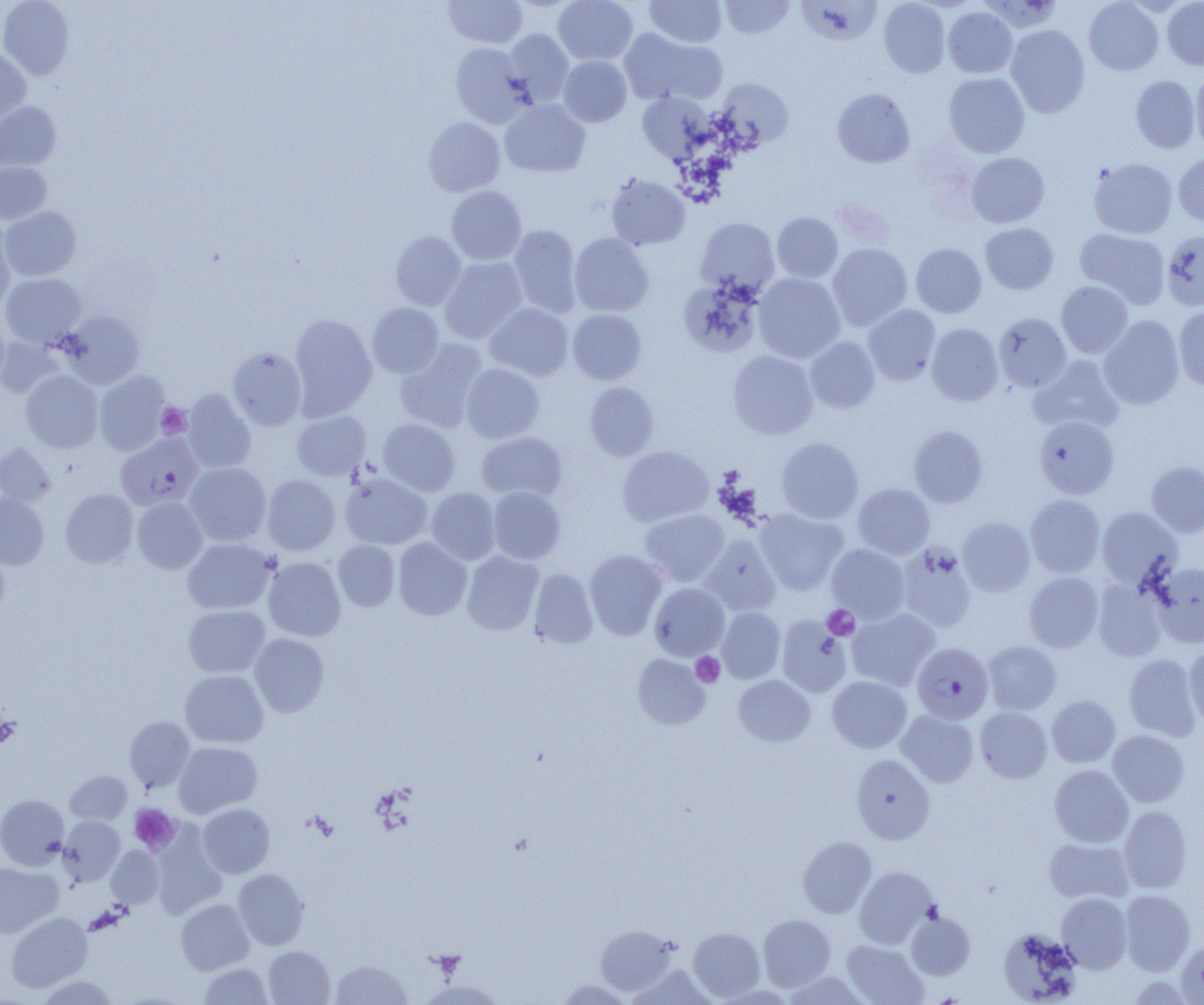 Approximate bounding boxes as named x1/y1/x2/y2 corners in pixels. Platelet locations: (x1=156, y1=403, x2=191, y2=439), (x1=822, y1=605, x2=859, y2=640), (x1=691, y1=652, x2=725, y2=687), (x1=0, y1=715, x2=20, y2=748), (x1=129, y1=804, x2=180, y2=854). Uninfected red blood cell locations: (x1=0, y1=0, x2=74, y2=80), (x1=444, y1=0, x2=527, y2=48), (x1=553, y1=0, x2=637, y2=65), (x1=645, y1=0, x2=726, y2=48), (x1=720, y1=0, x2=794, y2=38), (x1=879, y1=0, x2=950, y2=77), (x1=1084, y1=0, x2=1164, y2=76), (x1=797, y1=1, x2=881, y2=45), (x1=1162, y1=1, x2=1204, y2=70), (x1=943, y1=7, x2=1017, y2=78), (x1=1006, y1=25, x2=1090, y2=117), (x1=618, y1=28, x2=726, y2=107), (x1=504, y1=29, x2=574, y2=105), (x1=449, y1=43, x2=533, y2=127), (x1=0, y1=48, x2=31, y2=126), (x1=558, y1=55, x2=632, y2=127), (x1=1191, y1=69, x2=1204, y2=152), (x1=943, y1=72, x2=1030, y2=158), (x1=1131, y1=76, x2=1201, y2=154), (x1=716, y1=78, x2=794, y2=148), (x1=832, y1=88, x2=915, y2=168), (x1=637, y1=92, x2=712, y2=162), (x1=499, y1=99, x2=590, y2=177), (x1=0, y1=101, x2=61, y2=171), (x1=423, y1=117, x2=505, y2=196), (x1=966, y1=153, x2=1049, y2=228), (x1=1173, y1=153, x2=1204, y2=227), (x1=1089, y1=158, x2=1177, y2=239), (x1=0, y1=162, x2=52, y2=224), (x1=606, y1=173, x2=690, y2=251), (x1=446, y1=186, x2=527, y2=265), (x1=1, y1=206, x2=81, y2=281), (x1=772, y1=212, x2=843, y2=282), (x1=695, y1=217, x2=780, y2=297), (x1=0, y1=220, x2=15, y2=311), (x1=980, y1=223, x2=1058, y2=294), (x1=508, y1=225, x2=582, y2=318), (x1=1075, y1=228, x2=1170, y2=308), (x1=1161, y1=230, x2=1204, y2=311), (x1=390, y1=231, x2=466, y2=310), (x1=569, y1=233, x2=654, y2=317), (x1=827, y1=243, x2=913, y2=330), (x1=911, y1=243, x2=986, y2=318), (x1=439, y1=256, x2=528, y2=343), (x1=1, y1=273, x2=86, y2=347), (x1=753, y1=273, x2=845, y2=363), (x1=679, y1=277, x2=764, y2=358), (x1=1056, y1=281, x2=1133, y2=358), (x1=367, y1=303, x2=443, y2=378), (x1=485, y1=303, x2=574, y2=381), (x1=863, y1=305, x2=941, y2=385), (x1=1174, y1=306, x2=1204, y2=392), (x1=567, y1=309, x2=647, y2=385), (x1=578, y1=309, x2=652, y2=459), (x1=61, y1=310, x2=145, y2=388), (x1=289, y1=313, x2=377, y2=420), (x1=993, y1=313, x2=1071, y2=392), (x1=1098, y1=315, x2=1184, y2=409), (x1=0, y1=316, x2=9, y2=390), (x1=926, y1=323, x2=1003, y2=406), (x1=0, y1=335, x2=63, y2=398), (x1=805, y1=336, x2=880, y2=413), (x1=395, y1=340, x2=488, y2=432), (x1=228, y1=347, x2=307, y2=430), (x1=727, y1=350, x2=818, y2=439), (x1=1029, y1=355, x2=1124, y2=434), (x1=461, y1=363, x2=545, y2=443), (x1=21, y1=370, x2=103, y2=453), (x1=94, y1=371, x2=171, y2=455), (x1=585, y1=381, x2=659, y2=460), (x1=181, y1=389, x2=256, y2=473), (x1=292, y1=411, x2=370, y2=480), (x1=1034, y1=416, x2=1119, y2=499), (x1=378, y1=419, x2=460, y2=496), (x1=909, y1=425, x2=988, y2=507), (x1=476, y1=431, x2=567, y2=502), (x1=777, y1=437, x2=864, y2=523), (x1=0, y1=443, x2=55, y2=506), (x1=617, y1=446, x2=714, y2=526), (x1=1146, y1=460, x2=1204, y2=537), (x1=184, y1=462, x2=271, y2=546), (x1=340, y1=471, x2=432, y2=549), (x1=262, y1=474, x2=340, y2=555), (x1=852, y1=483, x2=934, y2=559), (x1=487, y1=486, x2=566, y2=564), (x1=426, y1=487, x2=501, y2=565), (x1=60, y1=488, x2=138, y2=568), (x1=0, y1=493, x2=49, y2=569), (x1=1025, y1=494, x2=1105, y2=577), (x1=132, y1=497, x2=207, y2=573), (x1=1097, y1=507, x2=1181, y2=588), (x1=639, y1=509, x2=729, y2=587), (x1=754, y1=509, x2=848, y2=594), (x1=957, y1=516, x2=1036, y2=596), (x1=700, y1=534, x2=781, y2=615), (x1=182, y1=537, x2=276, y2=614), (x1=393, y1=537, x2=472, y2=620), (x1=333, y1=540, x2=399, y2=611), (x1=826, y1=543, x2=909, y2=623), (x1=897, y1=544, x2=976, y2=632), (x1=0, y1=548, x2=9, y2=617), (x1=584, y1=549, x2=667, y2=639), (x1=462, y1=550, x2=544, y2=635), (x1=263, y1=557, x2=345, y2=641), (x1=1151, y1=562, x2=1204, y2=647), (x1=529, y1=568, x2=598, y2=649), (x1=1024, y1=572, x2=1103, y2=652), (x1=1092, y1=580, x2=1167, y2=661), (x1=649, y1=582, x2=729, y2=660), (x1=183, y1=605, x2=270, y2=678), (x1=717, y1=607, x2=786, y2=683), (x1=847, y1=608, x2=939, y2=691), (x1=776, y1=616, x2=852, y2=698), (x1=250, y1=634, x2=329, y2=716), (x1=983, y1=640, x2=1062, y2=714), (x1=1184, y1=645, x2=1204, y2=728), (x1=1124, y1=653, x2=1201, y2=741), (x1=633, y1=654, x2=709, y2=729), (x1=180, y1=670, x2=268, y2=748), (x1=734, y1=675, x2=815, y2=746), (x1=827, y1=676, x2=912, y2=753), (x1=1047, y1=695, x2=1121, y2=767), (x1=975, y1=707, x2=1052, y2=783), (x1=896, y1=709, x2=978, y2=787), (x1=124, y1=716, x2=195, y2=792), (x1=1107, y1=730, x2=1190, y2=807), (x1=173, y1=741, x2=262, y2=817), (x1=851, y1=754, x2=935, y2=844), (x1=1049, y1=765, x2=1134, y2=848), (x1=65, y1=770, x2=132, y2=824), (x1=0, y1=795, x2=69, y2=869), (x1=197, y1=803, x2=275, y2=878), (x1=1119, y1=805, x2=1193, y2=893), (x1=58, y1=815, x2=125, y2=886), (x1=150, y1=827, x2=226, y2=918), (x1=798, y1=836, x2=877, y2=917), (x1=1044, y1=837, x2=1134, y2=903), (x1=106, y1=846, x2=164, y2=908), (x1=0, y1=861, x2=62, y2=937), (x1=854, y1=867, x2=937, y2=948), (x1=233, y1=868, x2=309, y2=949), (x1=1120, y1=890, x2=1195, y2=975), (x1=1056, y1=893, x2=1132, y2=972), (x1=176, y1=899, x2=254, y2=974), (x1=6, y1=912, x2=92, y2=991), (x1=906, y1=912, x2=975, y2=979), (x1=758, y1=914, x2=835, y2=991), (x1=595, y1=925, x2=675, y2=994), (x1=688, y1=927, x2=765, y2=1000), (x1=998, y1=928, x2=1082, y2=1004), (x1=841, y1=939, x2=927, y2=1005), (x1=1175, y1=939, x2=1204, y2=1004), (x1=263, y1=946, x2=335, y2=1005), (x1=331, y1=959, x2=411, y2=1004), (x1=199, y1=963, x2=272, y2=1004), (x1=783, y1=971, x2=869, y2=1004), (x1=37, y1=974, x2=119, y2=1005), (x1=556, y1=979, x2=632, y2=1004), (x1=419, y1=980, x2=503, y2=1004). Plasmodium falciparum-infected red blood cell locations: (x1=116, y1=434, x2=203, y2=511), (x1=912, y1=642, x2=993, y2=724). Slide-level diagnosis: Plasmodium falciparum. 1000x magnification. Thin blood film. One field of a larger specimen. Image is 1204×1005 pixels. Light microscopy.